Give the extent of all Plasmodium malariae-infected red blood cells.
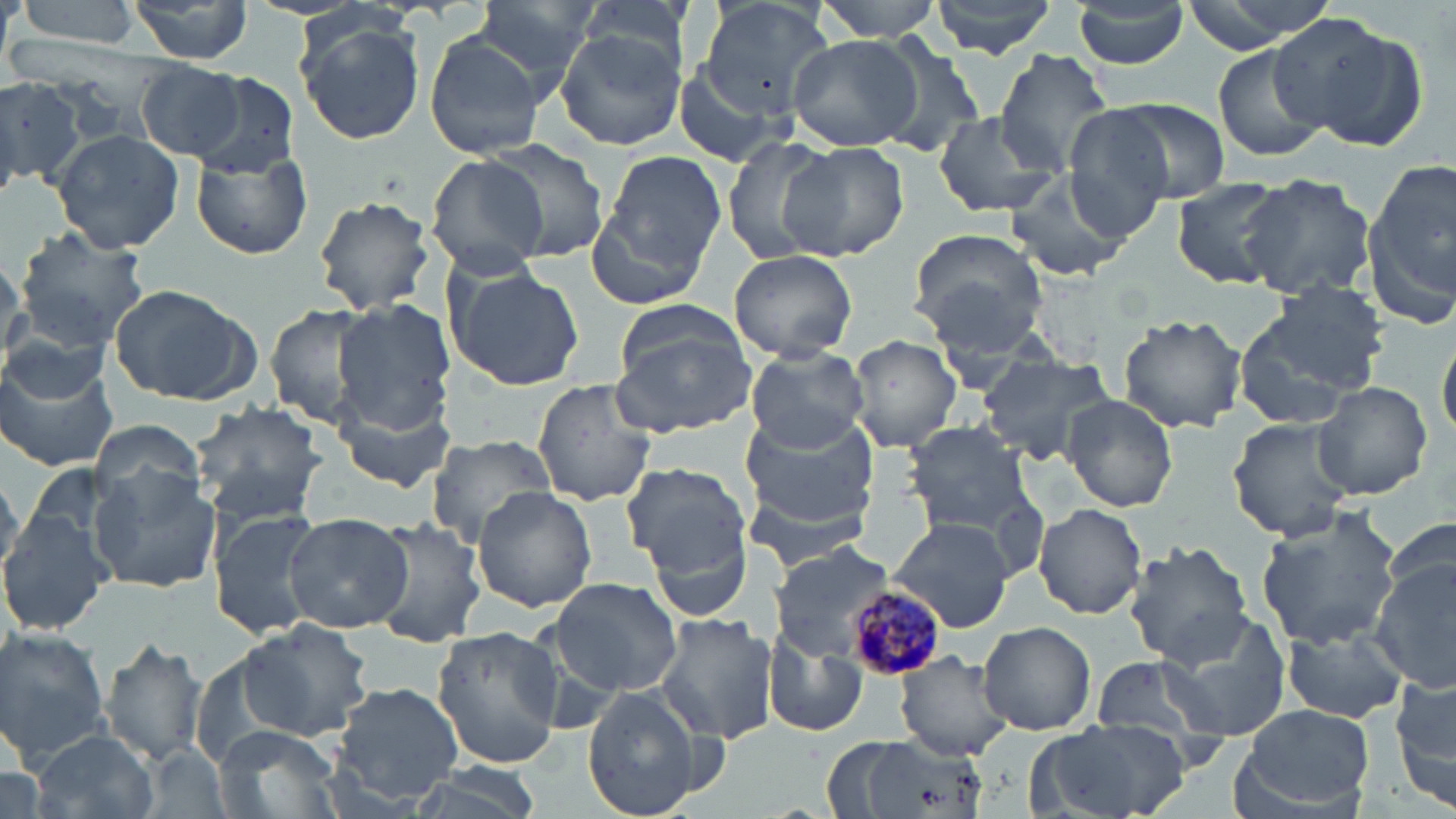
Approximate bounding boxes as named x1/y1/x2/y2 corners in pixels.
Plasmodium malariae-infected red blood cells: (x1=841, y1=585, x2=941, y2=682).

slide-level diagnosis = Plasmodium malariae
magnification = 1000x
uninfected red blood cell locations = approximate bounding boxes as named x1/y1/x2/y2 corners in pixels: (x1=13, y1=0, x2=150, y2=46), (x1=469, y1=0, x2=601, y2=91), (x1=573, y1=0, x2=690, y2=71), (x1=695, y1=0, x2=838, y2=116), (x1=810, y1=0, x2=945, y2=40), (x1=928, y1=0, x2=1059, y2=57), (x1=1179, y1=0, x2=1336, y2=51), (x1=126, y1=1, x2=259, y2=63), (x1=1071, y1=2, x2=1190, y2=69), (x1=1275, y1=16, x2=1425, y2=149), (x1=295, y1=21, x2=427, y2=146), (x1=554, y1=30, x2=686, y2=151), (x1=784, y1=31, x2=924, y2=151), (x1=422, y1=33, x2=549, y2=159), (x1=869, y1=36, x2=989, y2=159), (x1=891, y1=41, x2=1082, y2=171), (x1=1210, y1=44, x2=1328, y2=163), (x1=992, y1=49, x2=1115, y2=178), (x1=669, y1=61, x2=788, y2=169), (x1=139, y1=62, x2=247, y2=159), (x1=190, y1=73, x2=300, y2=177), (x1=0, y1=76, x2=85, y2=190), (x1=1110, y1=98, x2=1231, y2=204), (x1=1060, y1=108, x2=1174, y2=237), (x1=930, y1=111, x2=1060, y2=219), (x1=50, y1=129, x2=184, y2=253), (x1=482, y1=137, x2=611, y2=261), (x1=722, y1=138, x2=835, y2=265), (x1=780, y1=141, x2=909, y2=261), (x1=592, y1=147, x2=728, y2=288), (x1=190, y1=148, x2=313, y2=261), (x1=425, y1=153, x2=550, y2=279), (x1=1363, y1=161, x2=1456, y2=321), (x1=1004, y1=173, x2=1130, y2=282), (x1=1237, y1=173, x2=1376, y2=301), (x1=1169, y1=176, x2=1293, y2=288), (x1=315, y1=195, x2=436, y2=314), (x1=14, y1=227, x2=149, y2=348), (x1=907, y1=227, x2=1049, y2=344), (x1=728, y1=248, x2=859, y2=362), (x1=0, y1=257, x2=28, y2=363), (x1=445, y1=262, x2=584, y2=391), (x1=107, y1=283, x2=260, y2=405), (x1=613, y1=297, x2=746, y2=389), (x1=1233, y1=297, x2=1379, y2=428), (x1=332, y1=299, x2=456, y2=430), (x1=263, y1=306, x2=378, y2=426), (x1=1117, y1=315, x2=1247, y2=433), (x1=610, y1=326, x2=758, y2=435), (x1=849, y1=335, x2=963, y2=452), (x1=1437, y1=337, x2=1455, y2=443), (x1=745, y1=345, x2=868, y2=452), (x1=0, y1=352, x2=119, y2=473), (x1=976, y1=352, x2=1117, y2=463), (x1=531, y1=379, x2=659, y2=504), (x1=1311, y1=381, x2=1433, y2=501), (x1=332, y1=392, x2=458, y2=494), (x1=1061, y1=394, x2=1179, y2=512), (x1=187, y1=401, x2=331, y2=521), (x1=739, y1=409, x2=880, y2=527), (x1=1227, y1=417, x2=1357, y2=541), (x1=89, y1=420, x2=207, y2=515), (x1=901, y1=420, x2=1035, y2=533), (x1=424, y1=434, x2=559, y2=545), (x1=625, y1=464, x2=751, y2=581), (x1=89, y1=470, x2=221, y2=592), (x1=739, y1=482, x2=881, y2=574), (x1=471, y1=486, x2=598, y2=612), (x1=1033, y1=502, x2=1148, y2=620), (x1=643, y1=503, x2=756, y2=626), (x1=1, y1=507, x2=113, y2=635), (x1=209, y1=507, x2=325, y2=641), (x1=1253, y1=508, x2=1405, y2=650), (x1=283, y1=513, x2=411, y2=634), (x1=1380, y1=513, x2=1453, y2=598), (x1=364, y1=516, x2=486, y2=649), (x1=888, y1=516, x2=1017, y2=633), (x1=1126, y1=541, x2=1254, y2=667), (x1=769, y1=544, x2=893, y2=658), (x1=1373, y1=553, x2=1456, y2=692), (x1=547, y1=577, x2=685, y2=697), (x1=1158, y1=611, x2=1294, y2=740), (x1=655, y1=614, x2=779, y2=743), (x1=237, y1=618, x2=374, y2=742), (x1=978, y1=620, x2=1097, y2=735), (x1=1279, y1=621, x2=1410, y2=725), (x1=0, y1=627, x2=111, y2=762), (x1=432, y1=627, x2=563, y2=769), (x1=765, y1=631, x2=868, y2=738), (x1=100, y1=638, x2=209, y2=767), (x1=898, y1=652, x2=1016, y2=760), (x1=1092, y1=654, x2=1224, y2=745), (x1=1391, y1=675, x2=1456, y2=808), (x1=329, y1=682, x2=465, y2=807), (x1=583, y1=688, x2=704, y2=819), (x1=1237, y1=703, x2=1376, y2=815), (x1=1031, y1=720, x2=1192, y2=819), (x1=218, y1=725, x2=345, y2=819), (x1=29, y1=728, x2=157, y2=819), (x1=828, y1=732, x2=983, y2=819), (x1=398, y1=766, x2=553, y2=819)
stain = May-Grünwald-Giemsa
image size = 1456×819 pixels
field of view = one of a larger specimen
modality = optical microscopy
preparation = thin blood smear